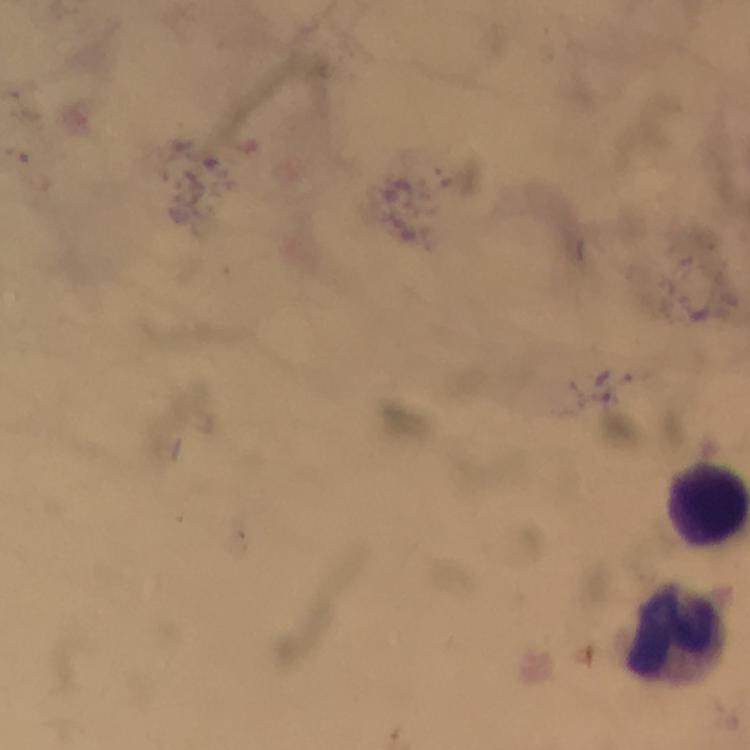
Approximate centers as [x, y] in pixels. Leukocyte locations: [710, 505], [677, 630]. A crop from one field of view. Immersion oil applied. Smartphone photograph taken through a microscope. Plasmodium parasites: none detected. Giemsa stain. At 100x magnification. Image is 750×750 pixels. From a malaria diagnostic workup. Thick blood film.